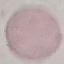
malaria status = uninfected
stain = Giemsa
image type = automatically extracted cell patch, resized to 64 × 64 pixels
capture = smartphone camera at the microscope eyepiece
preparation = thin blood film